Identify the parasite.
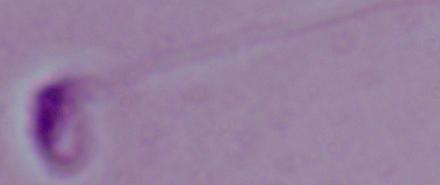
This is Leishmania.

magnification = 1000x
modality = photomicrograph